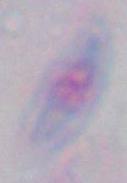
identification: Toxoplasma gondii
modality: photomicrograph
magnification: 1000x